Assess this cell for malaria.
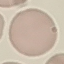
Uninfected.

Summary:
  - Capture: smartphone camera at the microscope eyepiece
  - Image type: cell patch, automatically extracted from a larger field of view and resized to 64 × 64 pixels
  - Preparation: thin smear
  - Stain: Giemsa